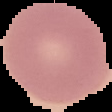
Summary:
  - Image size: 112×112 pixels
  - Malaria status: uninfected
  - Image type: cell region segmented out of the field of view; surrounding area masked to black
  - Preparation: thin blood smear